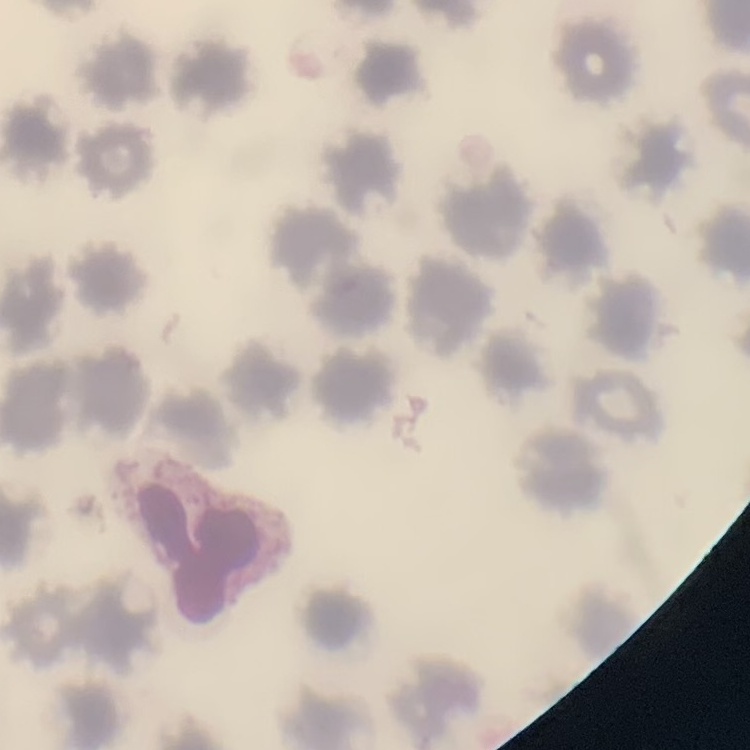

{
  "red_blood_cell_morphology": "no rouleaux formation",
  "preparation": "thin blood film",
  "image_type": "one tile cut from a larger photomicrograph",
  "stain": "Field's or Giemsa"
}